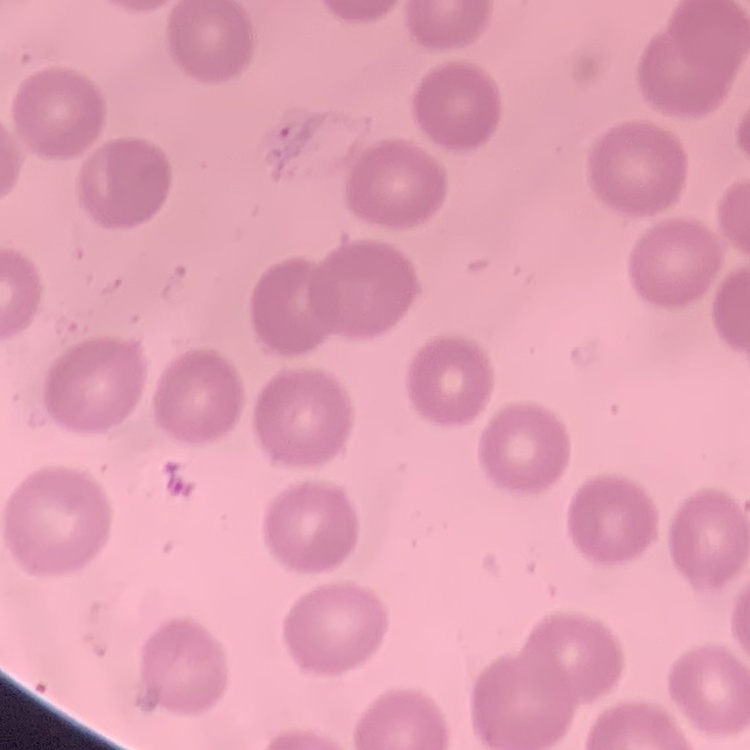

The red blood cells show no rouleaux formation. One tile cut from a larger photomicrograph. Stained with either Field's or Giemsa. Thin blood smear.